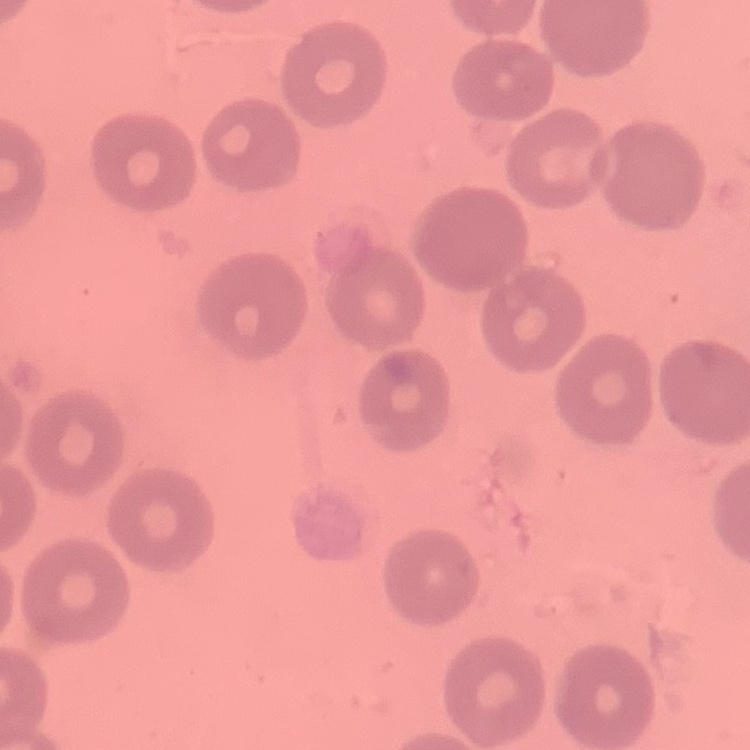
The erythrocytes show no rouleaux formation. Thin peripheral smear. Stained with either Field's or Giemsa. One tile cut from a larger photomicrograph.